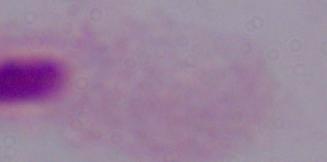
{
  "magnification": "1000x",
  "modality": "micrograph",
  "identification": "trichomonad"
}